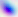
modality = micrograph
identification = Toxoplasma gondii
magnification = 400x